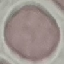

result = no malaria parasites seen
capture = smartphone through the microscope eyepiece
preparation = thin blood smear
stain = Giemsa
image type = automatically extracted cell patch, resized to 64 × 64 pixels